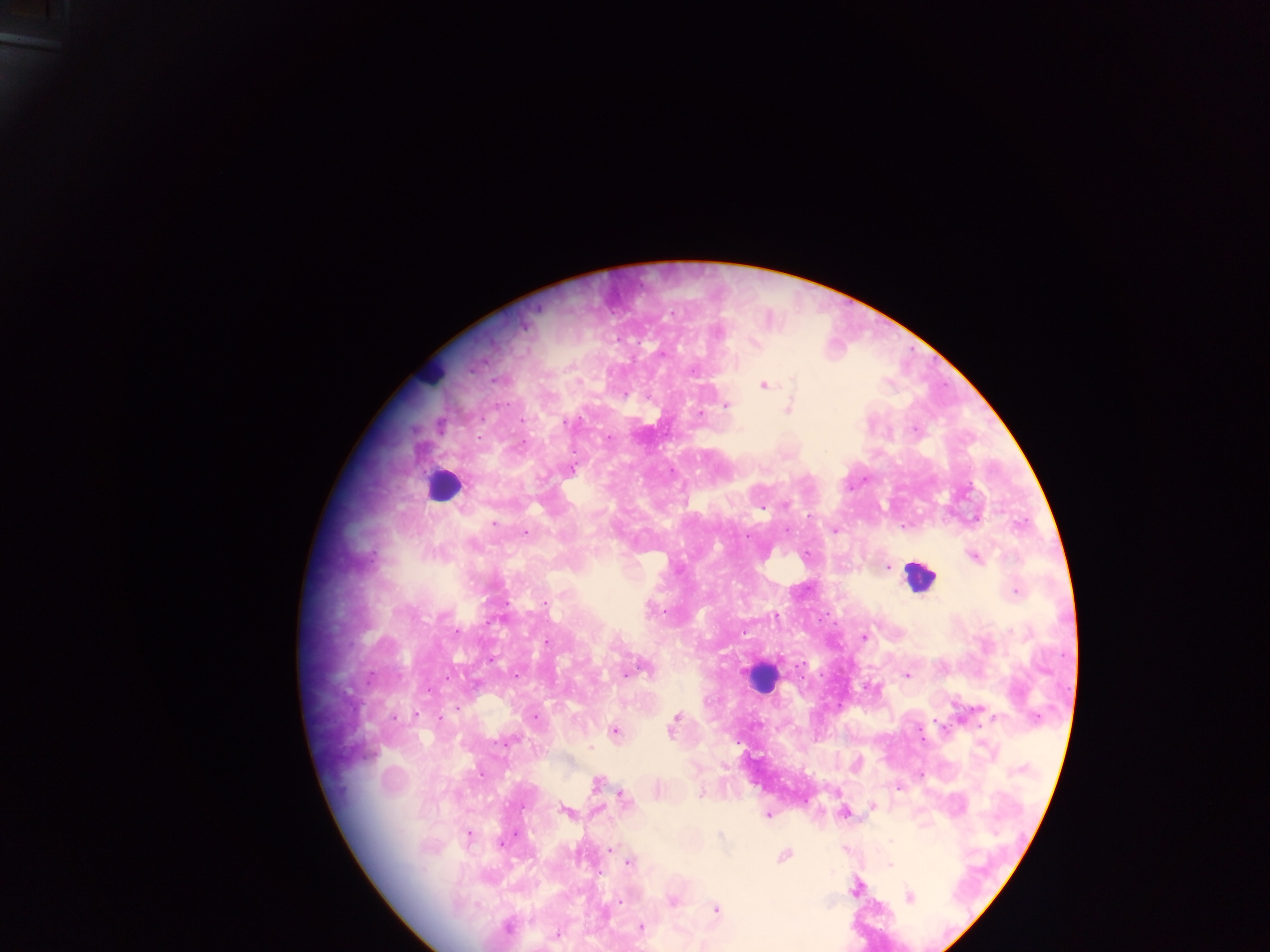

Approximate centers as (x, y) in pixels.
Summary:
  - Leukocyte locations: (432, 373), (444, 486), (921, 575), (761, 678)
  - Plasmodium parasite locations: (524, 329), (755, 344), (793, 376), (763, 385), (792, 389), (789, 402), (506, 406), (725, 406), (581, 418), (480, 420), (917, 429), (608, 441), (524, 442), (572, 470), (865, 478), (786, 504), (902, 527), (834, 530), (525, 531), (787, 531), (808, 553), (973, 558), (887, 567), (808, 587), (1013, 591), (547, 602), (507, 604), (663, 609), (819, 621), (457, 632), (864, 635), (544, 642), (644, 666), (625, 672), (370, 674), (517, 674), (821, 674), (909, 676), (429, 691), (456, 706), (414, 716), (443, 716), (392, 718), (439, 718), (677, 719), (935, 721), (673, 728), (615, 733), (923, 739), (590, 746), (924, 776), (595, 784), (898, 788), (701, 791), (623, 800), (875, 806), (564, 812), (768, 814), (719, 833), (468, 834), (893, 841), (504, 844), (609, 849), (844, 849), (785, 855), (628, 864), (890, 865), (854, 891), (910, 898), (621, 900), (672, 900), (717, 909), (508, 925), (641, 926), (557, 933)
  - Country: Ghana
  - Capture: mobile-phone photograph through a microscope
  - Preparation: thick blood film
  - Field of view: single
  - Image size: 1270×952 pixels